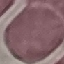 Result: negative for malaria parasites. Giemsa-stained preparation. Cell patch, automatically extracted from a larger field of view and resized to 64 × 64 pixels. Thin smear of blood. Acquired by smartphone through the microscope eyepiece.